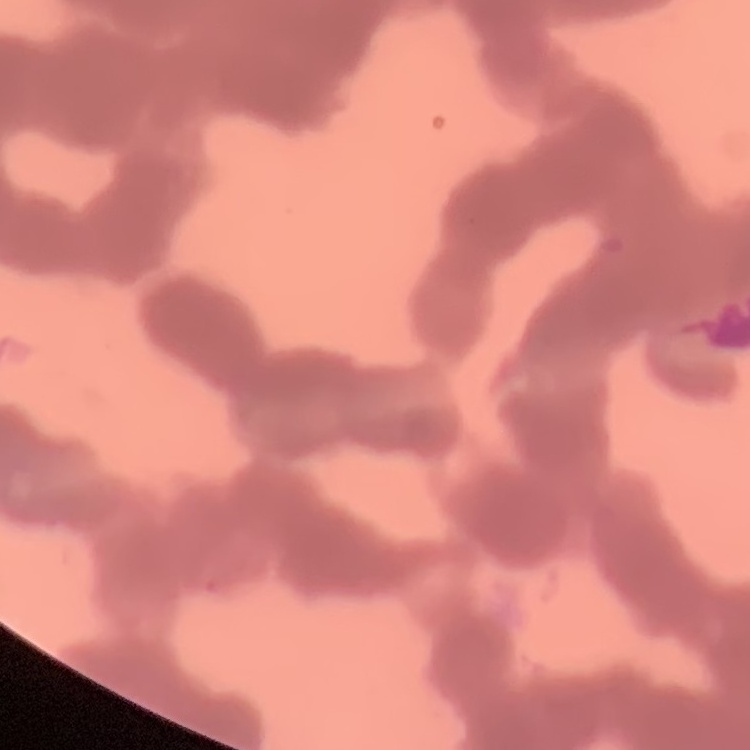

Summary:
  - Erythrocyte morphology: rouleaux formation
  - Preparation: thin blood smear
  - Stain: Field's or Giemsa
  - Image type: square crop of a larger photomicrograph